Identify the preparation type.
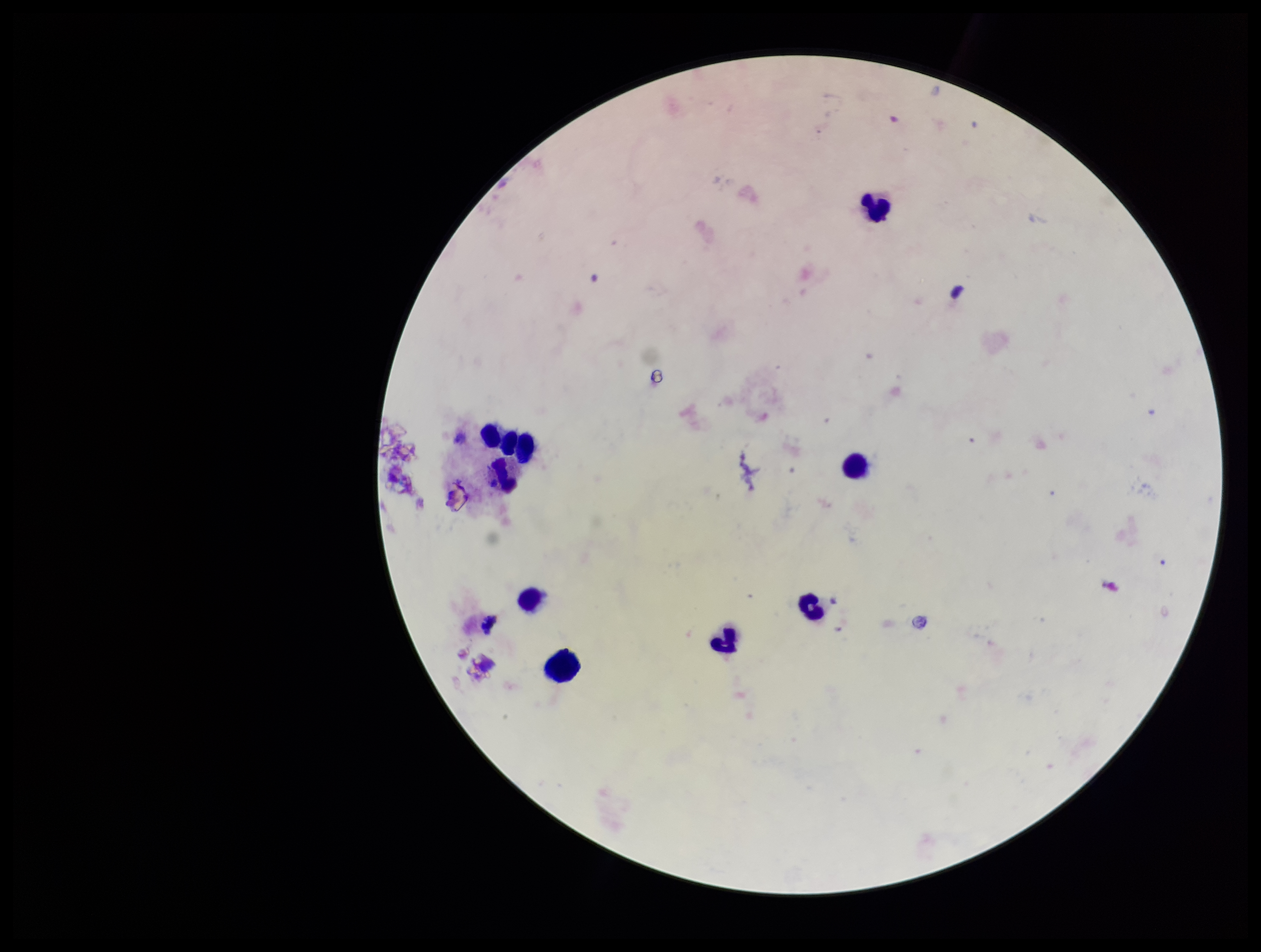

A thick smear.

field of view = single
stain = Giemsa
capture = smartphone photograph through the microscope eyepiece
Plasmodium parasites = none identified
parasite count = 0
image size = 1261×952 pixels
leukocyte count = 10
patient malaria status = negative